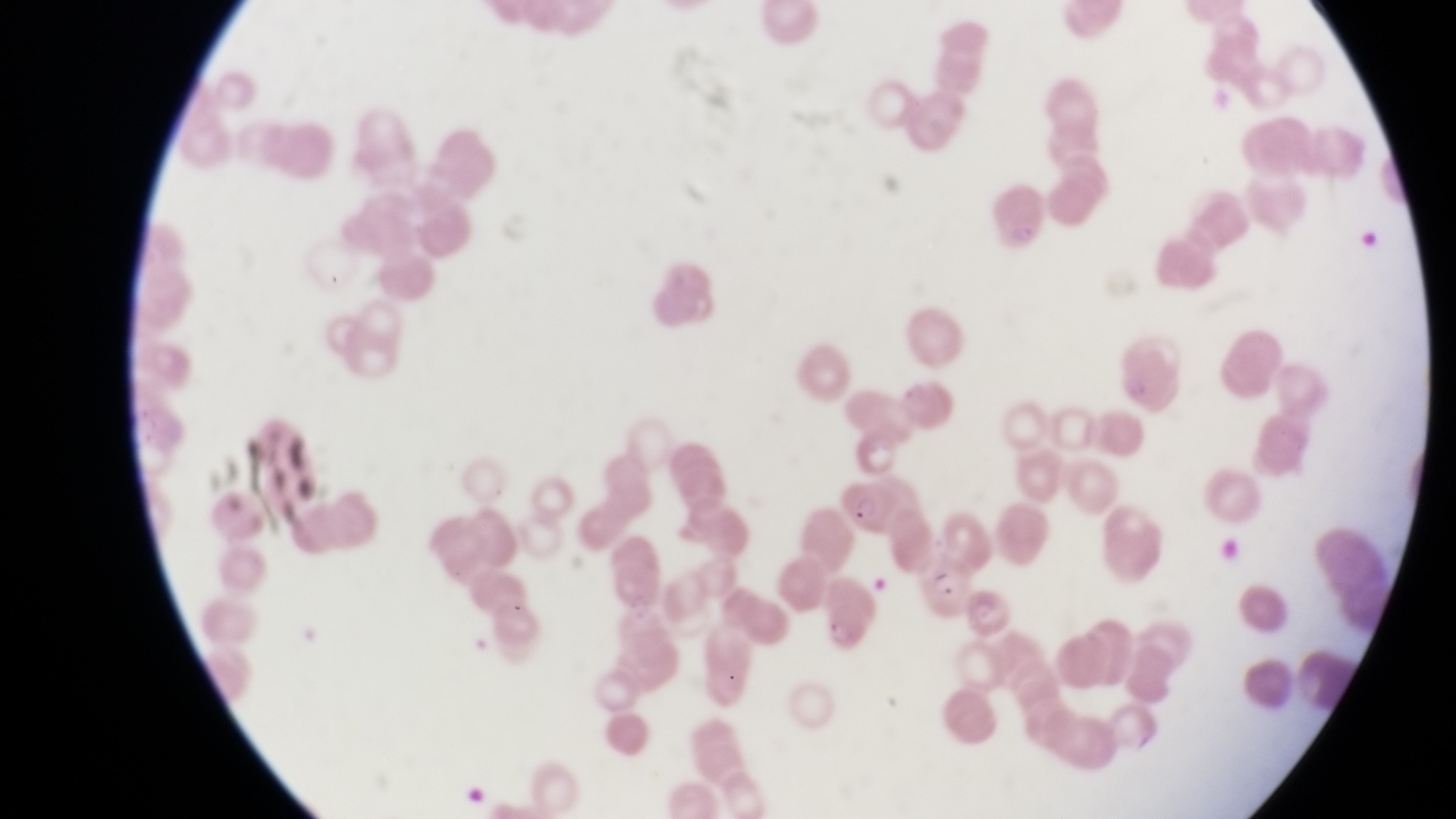

Approximate bounding boxes as [left, top, right, bottom] in pixels.
Summary:
  - Parasitised red blood cell locations: [832, 473, 892, 537], [918, 560, 967, 618]
  - Capture: smartphone photograph through the eyepiece of an Olympus CX-23 microscope
  - Preparation: thin blood smear
  - Field of view: single
  - Country: Uganda
  - Image size: 1456×819 pixels
  - Magnification: 1000x